Give the position of every malaria parasite.
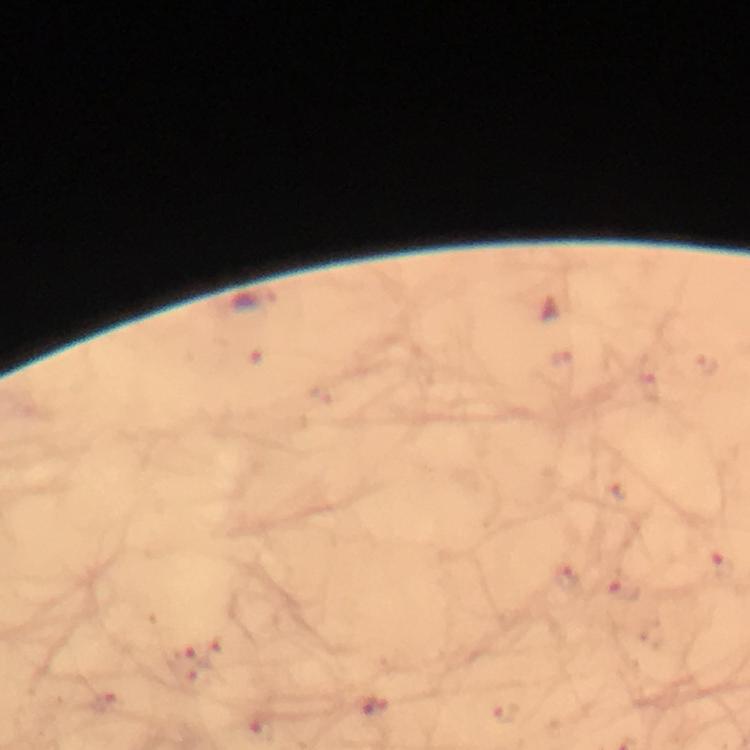
Approximate object centers, in pixels from the top-left corner.
Malaria parasites: (x=254, y=302).

magnification = 100x
cropped from = one field of view
stain = Giemsa
capture = smartphone mounted on the microscope
context = from a diagnostic examination for malaria
immersion oil = applied
preparation = thick blood smear
image size = 750×750 pixels